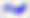

400x magnification. Toxoplasma gondii is seen. Micrograph.